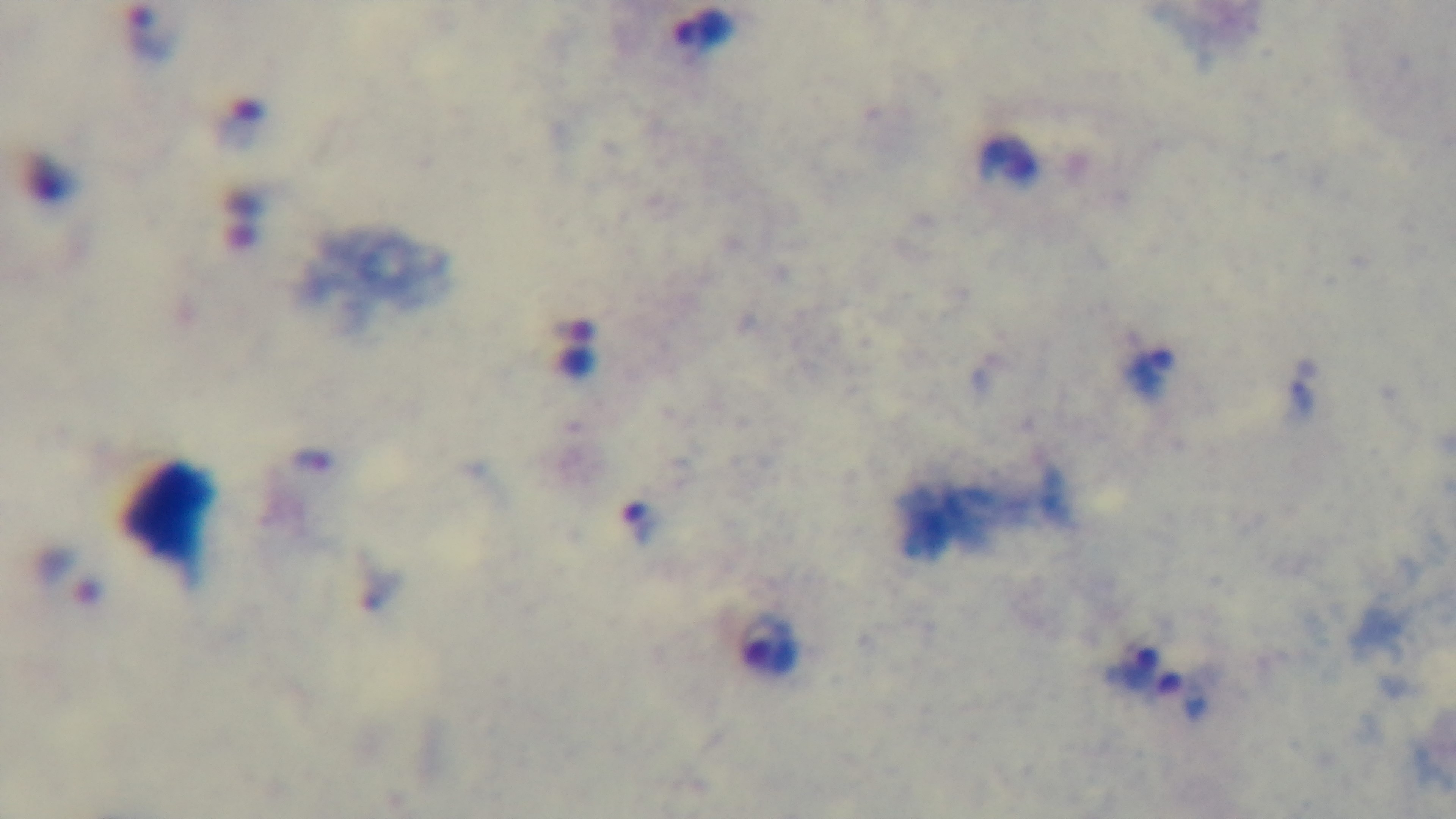
field_of_view: one from the slide
malaria_status: positive
preparation: thick
capture: mounted 4K digital camera
stain: Giemsa
modality: light microscopy
objective: 100x oil immersion